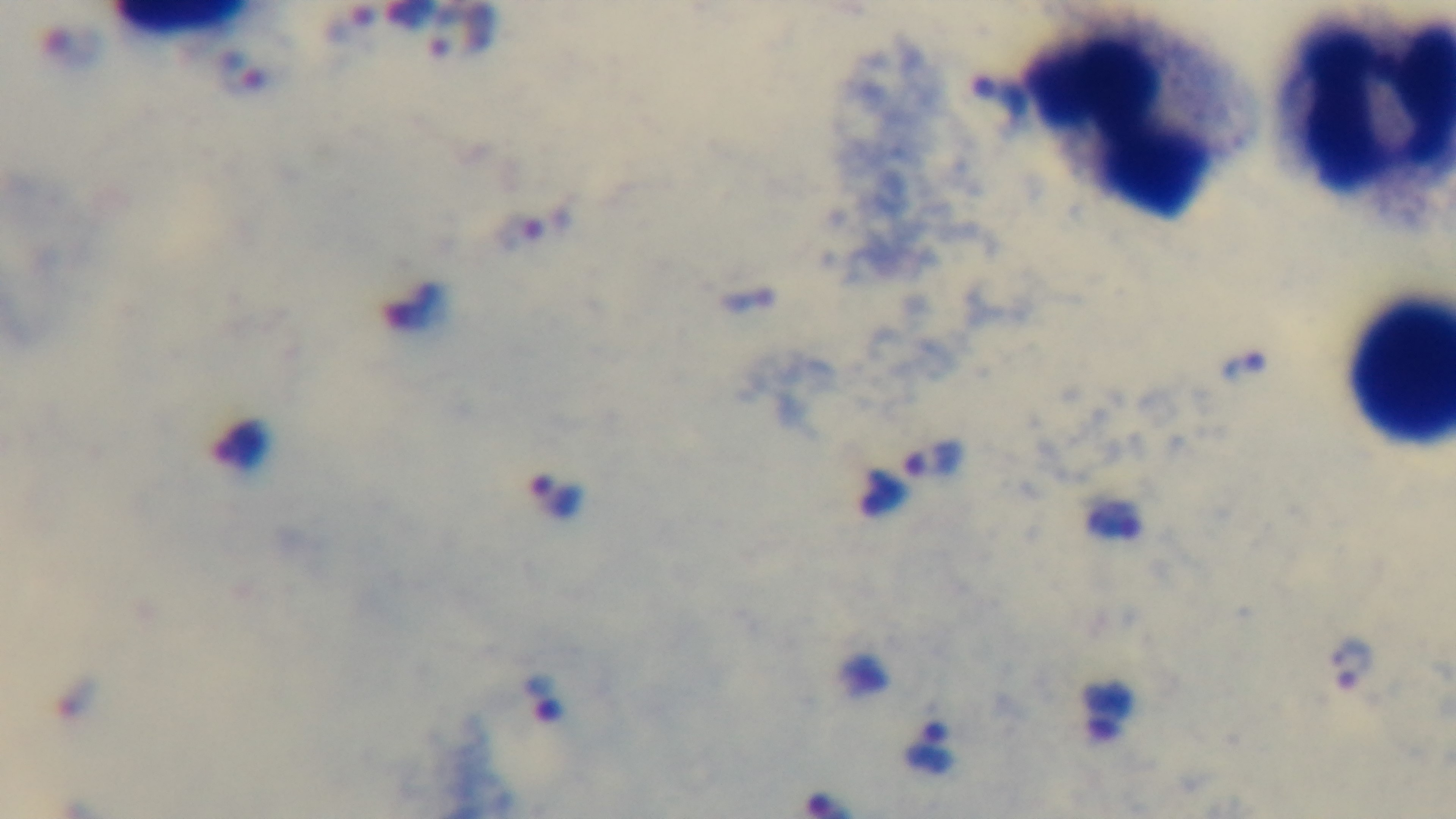

objective = 100x oil immersion
modality = light microscopy
capture = mounted 4K digital camera
stain = Giemsa
malaria status = positive
field of view = single
preparation = thick blood film